Point out each Plasmodium parasite.
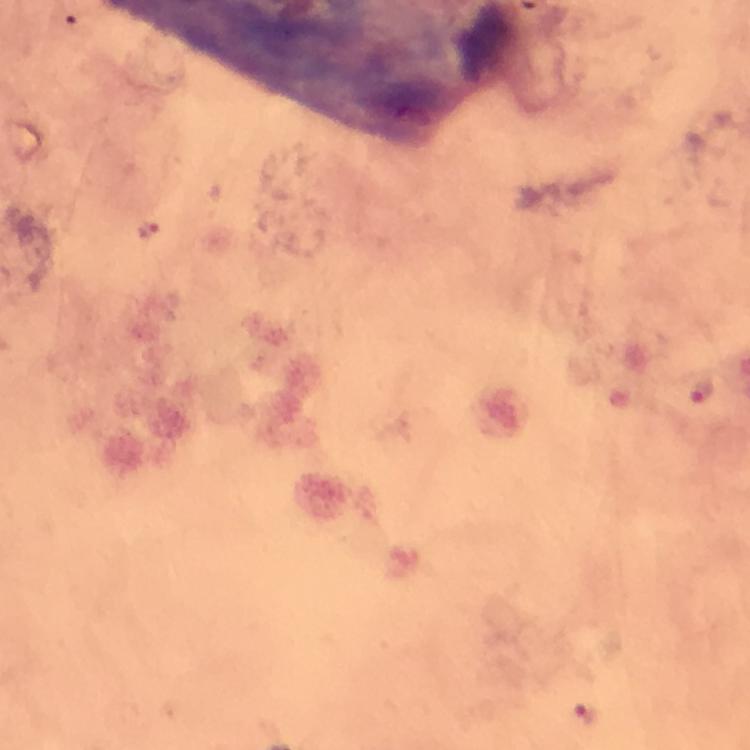
Approximate object centers, in pixels from the top-left corner.
Plasmodium parasites: (x=149, y=230), (x=700, y=391), (x=587, y=713).

Immersion oil applied. 100x magnification. Photographed through the microscope with a smartphone camera. Image is 750×750 pixels. From a diagnostic examination for malaria. A crop from one field of view. Thick blood film. Giemsa-stained preparation.